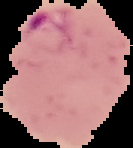

{
  "image_type": "cell region segmented out of the field of view; surrounding area masked to black",
  "malaria_status": "parasitized",
  "preparation": "thin blood smear",
  "image_size": "133×148 pixels"
}